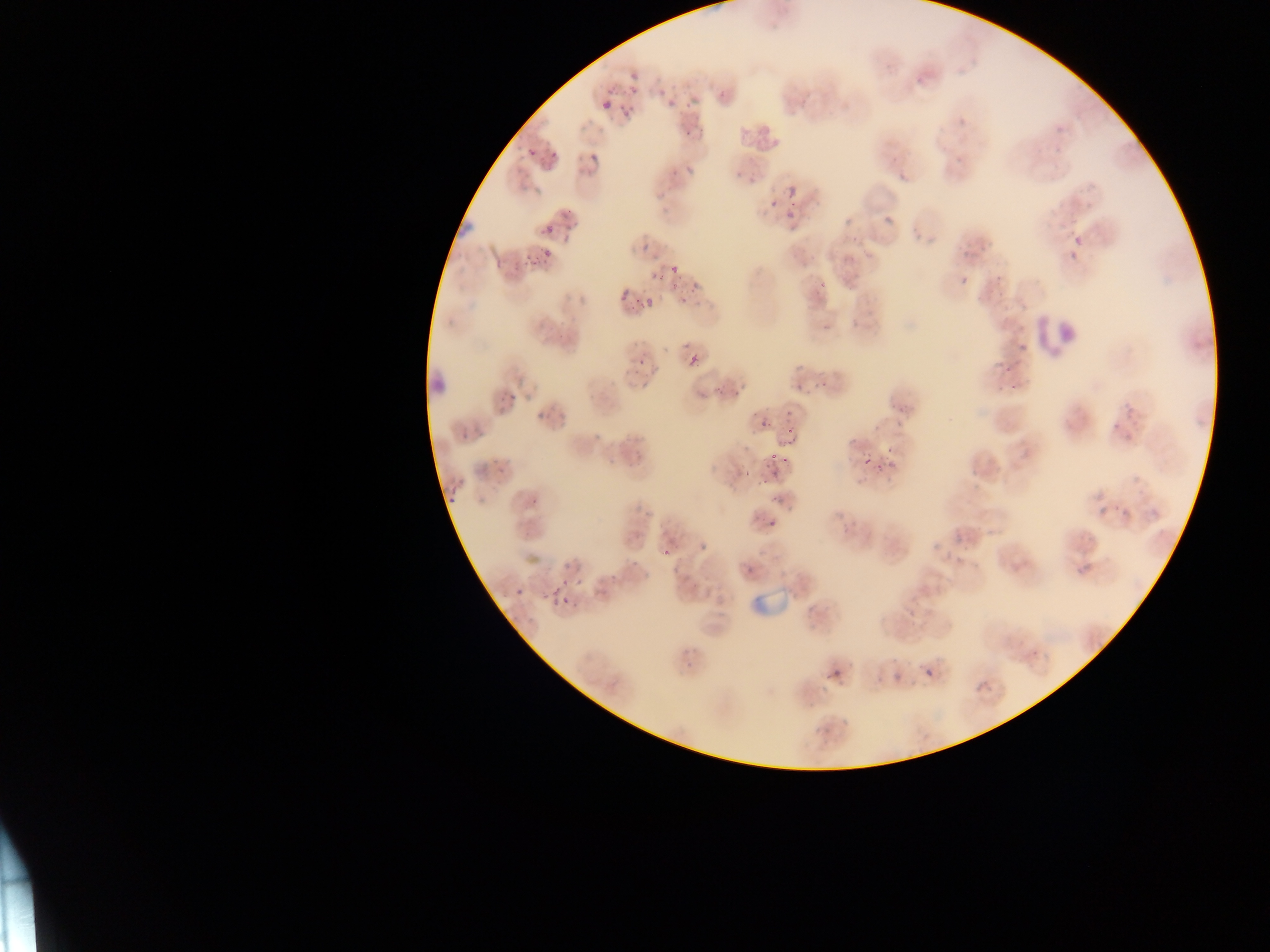
Approximate bounding boxes as (left, top, right, bottom) in pixels. Leukocyte locations: (1035, 312, 1082, 357), (423, 351, 445, 403). Plasmodium parasite locations: (628, 64, 645, 78), (715, 85, 735, 101), (664, 94, 682, 109), (596, 97, 618, 114), (622, 97, 632, 119), (750, 122, 787, 160), (677, 131, 695, 148), (518, 141, 536, 163), (545, 144, 559, 162), (581, 147, 604, 178), (682, 170, 697, 180), (729, 170, 752, 195), (893, 172, 908, 182), (781, 182, 794, 200), (529, 186, 546, 204), (654, 194, 663, 205), (766, 200, 778, 210), (882, 209, 904, 235), (786, 212, 797, 226), (838, 217, 856, 231), (561, 218, 579, 236), (536, 219, 558, 232), (633, 229, 654, 253), (1069, 233, 1083, 252), (537, 245, 560, 266), (960, 246, 970, 254), (516, 252, 534, 266), (1065, 253, 1079, 264), (670, 267, 684, 277), (958, 273, 979, 288), (649, 274, 663, 283), (811, 274, 833, 291), (993, 276, 1007, 289), (612, 289, 628, 299), (677, 289, 696, 305), (629, 301, 647, 311), (1014, 341, 1029, 351), (628, 352, 646, 371), (688, 354, 702, 369), (1002, 363, 1019, 378), (790, 365, 804, 375), (632, 376, 654, 395), (813, 376, 831, 391), (1006, 379, 1024, 397), (715, 383, 729, 396), (797, 383, 807, 390), (695, 388, 709, 402), (497, 389, 518, 411), (530, 401, 552, 427), (891, 403, 912, 417), (1118, 403, 1140, 421), (783, 417, 801, 444), (757, 418, 768, 435), (1106, 423, 1127, 440), (454, 428, 468, 446), (1122, 433, 1136, 444), (881, 439, 893, 461), (858, 447, 875, 471), (768, 455, 779, 468), (483, 460, 508, 480), (877, 461, 891, 478), (741, 463, 759, 477), (852, 482, 867, 492), (445, 486, 459, 504), (768, 494, 781, 502), (1090, 497, 1116, 514), (763, 510, 789, 530), (637, 511, 655, 527), (699, 541, 713, 555), (929, 541, 946, 553), (657, 545, 672, 560), (1075, 556, 1098, 578), (560, 560, 569, 571), (741, 561, 762, 579), (670, 565, 689, 581), (605, 567, 620, 584), (572, 577, 587, 590), (547, 584, 564, 603), (514, 587, 528, 602), (558, 594, 574, 610), (922, 665, 934, 676), (888, 667, 910, 685), (827, 670, 838, 682), (971, 676, 994, 694). Artifact (stain precipitate or debris) locations: (452, 182, 482, 238). Single field of view. Image is 1270×952 pixels. Mobile-phone photograph taken through the microscope. Thin blood film. Sample from Ghana.